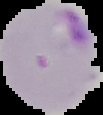

From a thin blood smear. Malaria status: parasitized. Cell region segmented out of the field of view; the surrounding area is masked to black. Image is 103×115 pixels.